Report the malaria status of this cell.
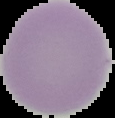
It is uninfected.

image type = segmented cell region on a black background
image size = 115×118 pixels
preparation = thin blood smear